Report the malaria status of this cell.
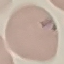
Uninfected.

Summary:
  - Capture: smartphone through the microscope eyepiece
  - Stain: Giemsa
  - Image type: automatically extracted cell patch, resized to 64 × 64 pixels
  - Preparation: thin blood smear